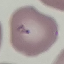

Malaria status: uninfected. Cell patch, automatically extracted from a larger field of view and resized to 64 × 64 pixels. Giemsa stain. Thin blood smear. Photographed with a smartphone camera at the microscope eyepiece.